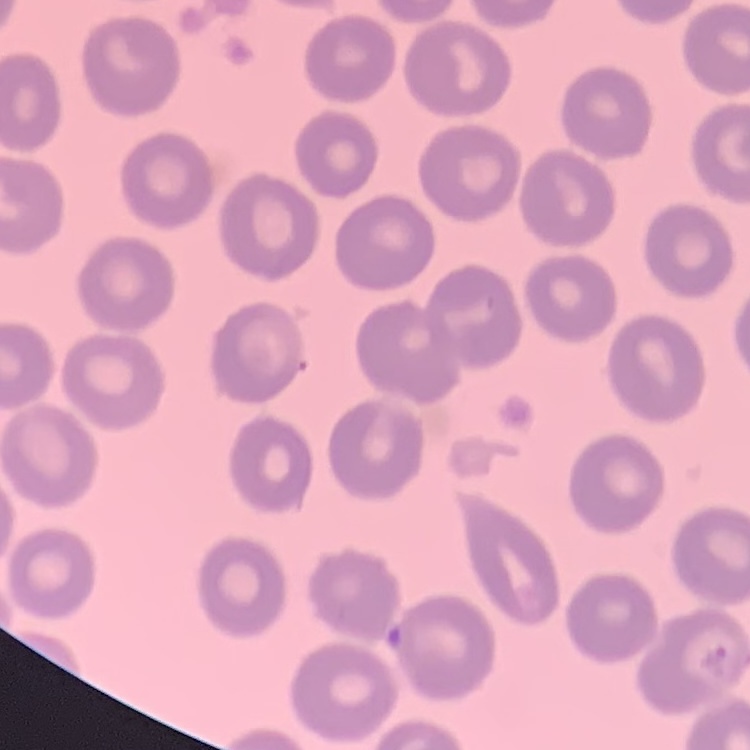

Summary:
  - Erythrocyte morphology: no rouleaux formation
  - Preparation: thin peripheral smear
  - Stain: Field's or Giemsa
  - Image type: square crop of a larger photomicrograph